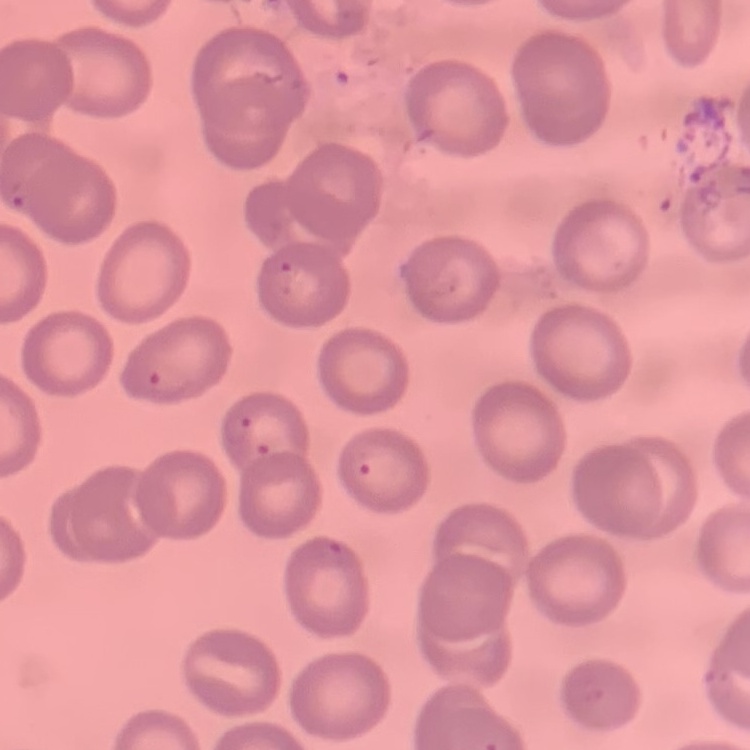
Summary:
  - Erythrocyte morphology: no rouleaux formation
  - Preparation: thin peripheral smear
  - Image type: square crop of a larger photomicrograph
  - Stain: Field's or Giemsa